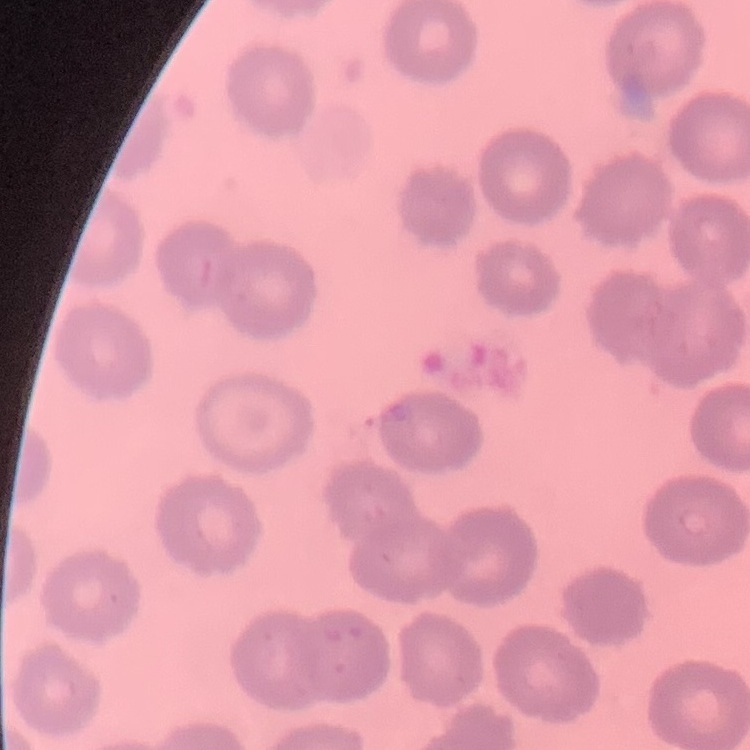
The red blood cells exhibit no rouleaux formation. Square crop of a larger photomicrograph. Thin blood film. Stained with either Field's or Giemsa.